Name the cell type shown.
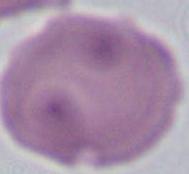
An erythrocyte.

Captured at 1000x magnification. Micrograph.